Assess the morphology of the red blood cells.
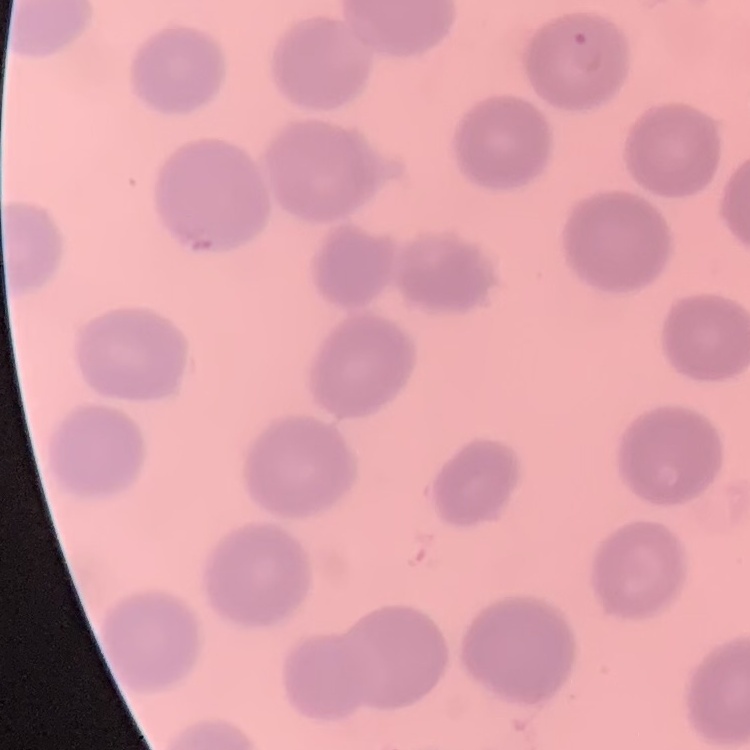

No rouleaux formation.

image type = one tile cut from a larger photomicrograph
stain = Field's or Giemsa
preparation = thin peripheral smear